Name the parasite shown.
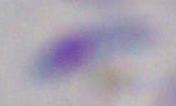

Toxoplasma gondii.

magnification: 1000x
modality: micrograph